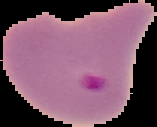 Image is 157×127 pixels. From a thin blood film. Result: malaria parasites detected. The area outside the segmented cell region is set to black.